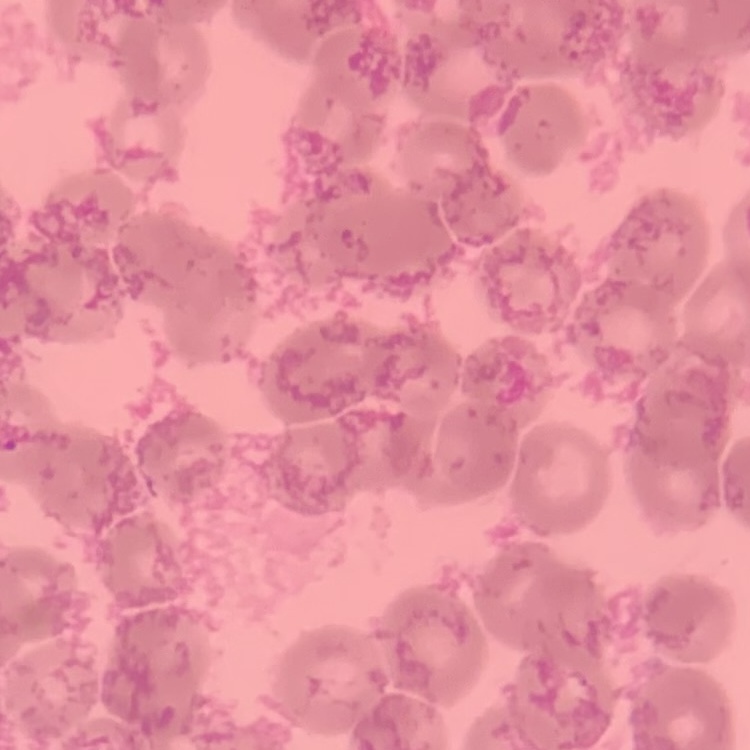
The erythrocytes exhibit rouleaux formation. Square crop of a larger photomicrograph. Stained with either Field's or Giemsa. Thin blood film.